Identify the cell.
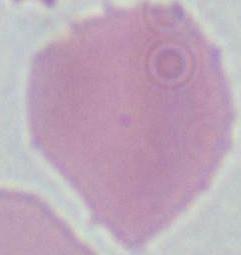
An erythrocyte.

magnification = 1000x
modality = micrograph